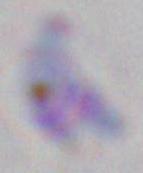

Micrograph. Captured at 1000x magnification. Toxoplasma gondii is seen.